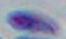

Summary:
  - Identification: Toxoplasma gondii
  - Magnification: 1000x
  - Modality: photomicrograph